Classify this cell by malaria status.
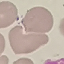

It is uninfected.

Summary:
  - Capture: smartphone camera at the microscope eyepiece
  - Preparation: thin blood film
  - Image type: automatically extracted cell patch, resized to 64 × 64 pixels
  - Stain: Giemsa